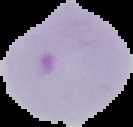
Image is 133×127 pixels. Malaria status: parasitized. Segmented cell region on a black background. From a thin blood smear.